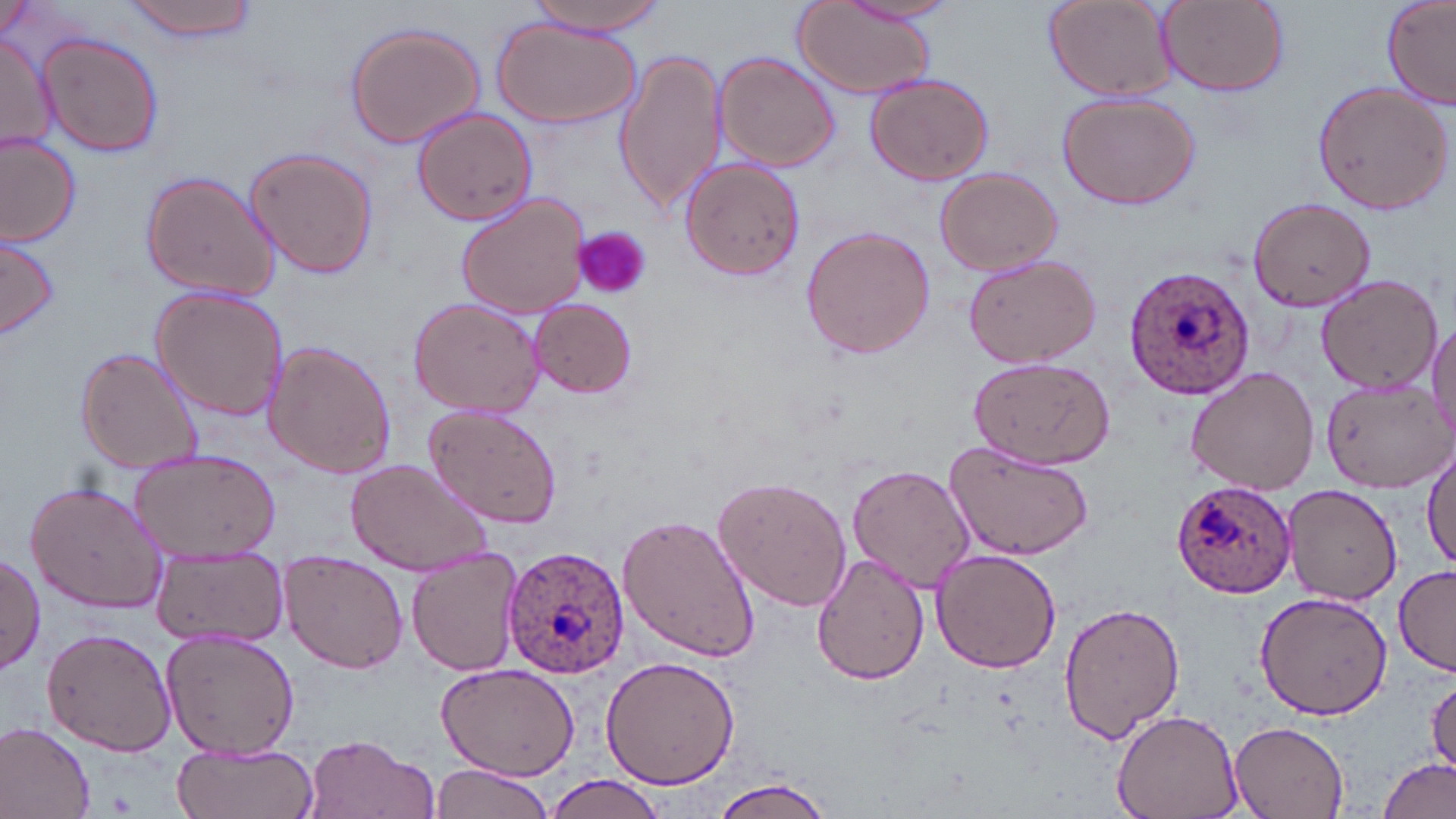
slide-level diagnosis = Plasmodium ovale
magnification = 1000x
stain = May-Grünwald-Giemsa
modality = light microscopy
image size = 1456×819 pixels
Plasmodium ovale-infected red blood cell locations = approximate bounding boxes as [x1, y1, x2, y2] in pixels: [1122, 265, 1258, 401], [1171, 481, 1299, 598], [502, 543, 630, 682]
preparation = thin blood smear
uninfected red blood cell locations = approximate bounding boxes as [x1, y1, x2, y2] in pixels: [124, 0, 259, 42], [525, 0, 668, 36], [1044, 0, 1176, 100], [1157, 0, 1289, 96], [1380, 0, 1456, 108], [843, 1, 958, 28], [0, 2, 43, 39], [792, 2, 936, 99], [488, 16, 640, 127], [343, 20, 486, 149], [0, 30, 57, 156], [36, 31, 164, 159], [614, 48, 727, 214], [713, 50, 842, 171], [865, 72, 994, 186], [1309, 81, 1453, 215], [1053, 90, 1203, 209], [411, 108, 540, 226], [0, 134, 81, 245], [244, 145, 379, 281], [679, 156, 805, 281], [935, 167, 1064, 277], [139, 170, 279, 303], [453, 190, 591, 319], [1248, 196, 1374, 314], [799, 223, 938, 362], [1, 231, 60, 338], [961, 252, 1102, 369], [1314, 273, 1441, 392], [149, 284, 291, 423], [408, 297, 544, 418], [528, 299, 638, 398], [1428, 319, 1456, 450], [263, 341, 399, 478], [74, 345, 203, 476], [968, 356, 1116, 470], [1186, 364, 1319, 496], [1320, 382, 1449, 492], [424, 404, 564, 530], [1422, 440, 1456, 570], [944, 442, 1093, 561], [127, 448, 283, 562], [344, 458, 493, 576], [847, 464, 975, 593], [712, 474, 853, 614], [25, 477, 168, 613], [1283, 483, 1402, 607], [618, 512, 761, 662], [151, 545, 289, 648], [405, 546, 526, 679], [929, 549, 1063, 674], [809, 550, 929, 683], [0, 551, 45, 674], [279, 551, 410, 675], [1394, 565, 1456, 674], [1254, 590, 1393, 719], [1058, 603, 1185, 742], [160, 626, 300, 760], [41, 627, 176, 755], [599, 656, 740, 791], [436, 664, 580, 782], [1427, 672, 1456, 778], [1111, 706, 1243, 819], [1228, 719, 1353, 819], [0, 721, 95, 818], [302, 733, 436, 819], [173, 741, 318, 819], [1379, 756, 1454, 819], [428, 762, 553, 819], [545, 775, 663, 817], [710, 776, 836, 818]
field of view = single
platelet locations = approximate bounding boxes as [x1, y1, x2, y2] in pixels: [578, 226, 655, 297]